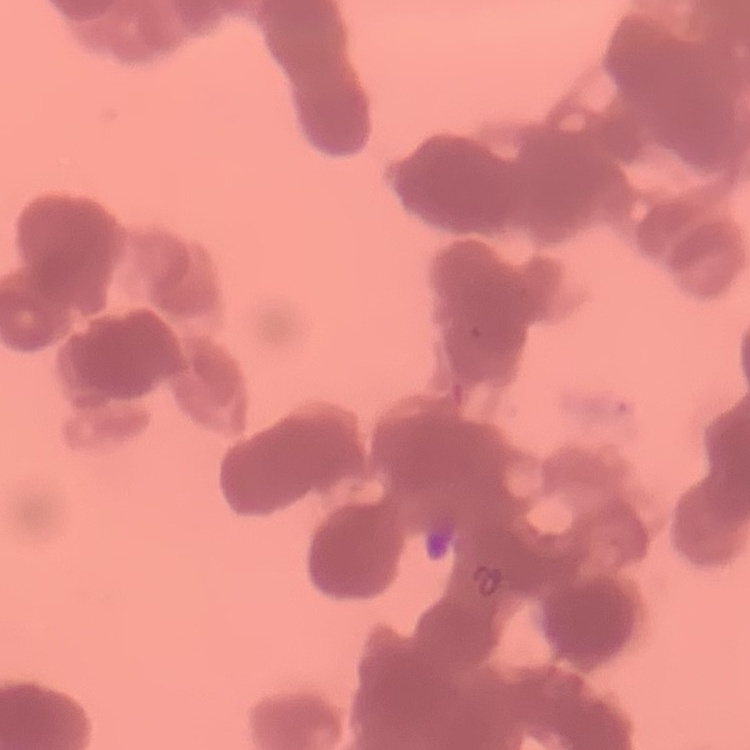

red blood cell morphology = rouleaux formation
preparation = thin blood film
image type = one tile cut from a larger photomicrograph
stain = Field's or Giemsa